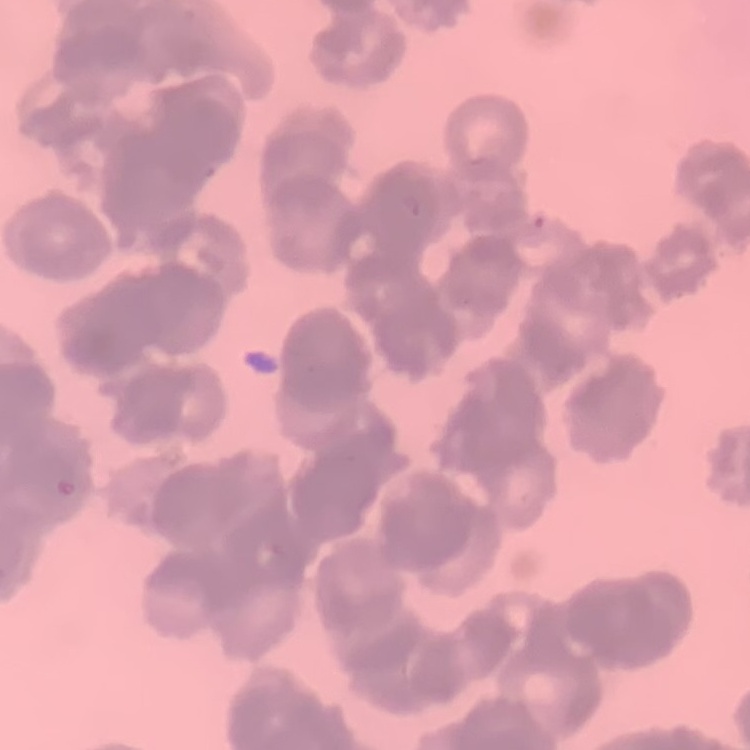
Summary:
  - Red blood cell morphology: rouleaux formation
  - Stain: Field's or Giemsa
  - Preparation: thin peripheral smear
  - Image type: square crop of a larger photomicrograph